Locate every Plasmodium ovale-infected red blood cell.
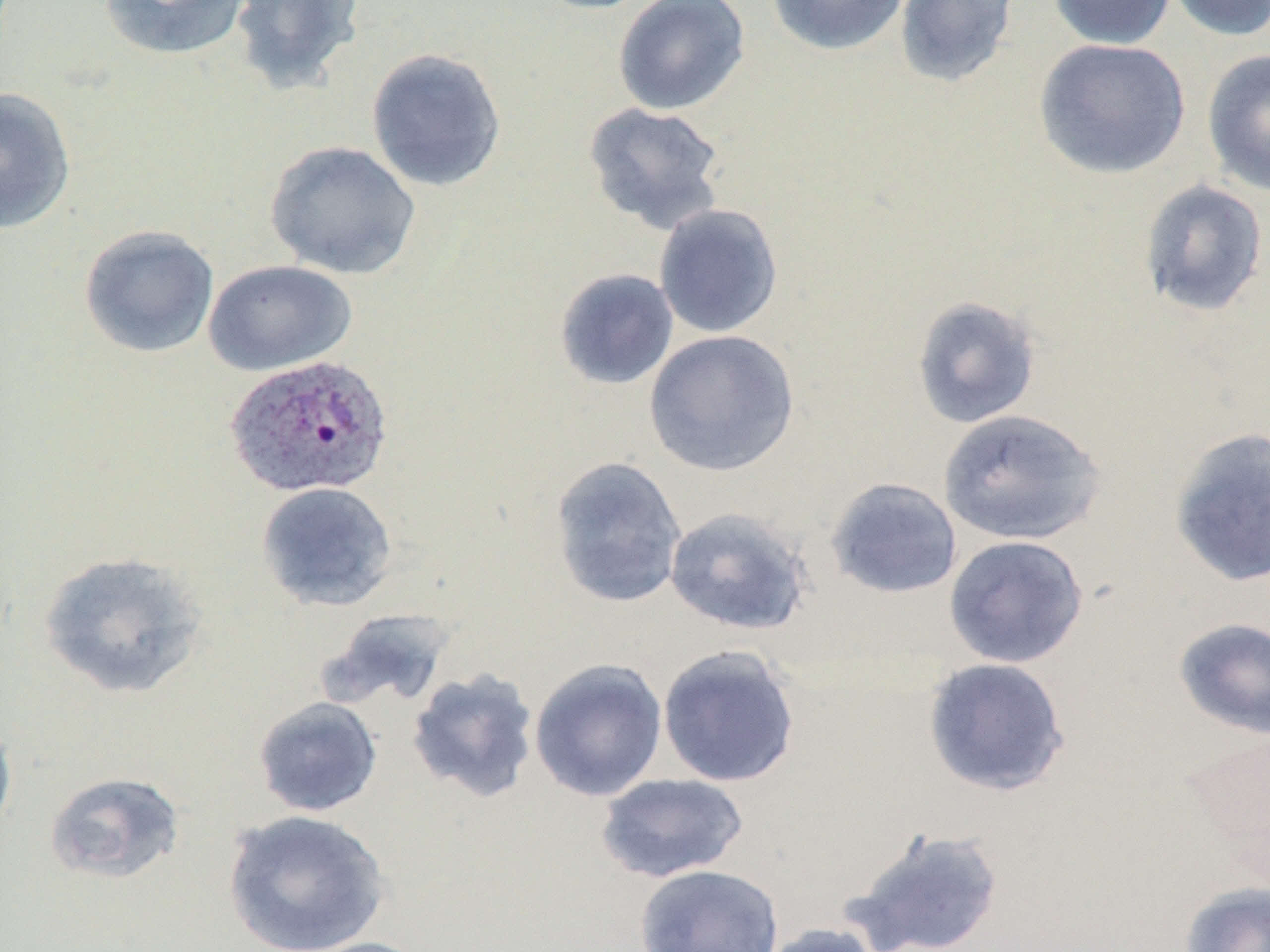

Approximate bounding boxes as (x1,y1)-(x2,y2) corner pairs in pixels.
Plasmodium ovale-infected red blood cells: (225,353)-(394,498).

Uninfected red blood cell locations: (98,0)-(252,62), (229,0)-(367,96), (528,0)-(658,14), (613,0)-(750,116), (765,0)-(910,57), (894,0)-(1020,88), (1047,0)-(1177,49), (1165,0)-(1270,42), (1033,37)-(1191,179), (365,47)-(507,192), (1202,48)-(1270,198), (0,86)-(77,235), (583,102)-(727,234), (264,140)-(421,280), (1138,179)-(1269,318), (653,203)-(784,338), (79,224)-(220,358), (203,260)-(358,376), (553,268)-(679,391), (911,295)-(1042,429), (643,329)-(800,477), (937,407)-(1105,546), (1168,426)-(1270,588), (548,455)-(688,609), (825,477)-(962,599), (256,481)-(398,611), (663,506)-(813,636), (943,535)-(1088,668), (38,550)-(208,700), (322,606)-(458,710), (1172,617)-(1270,739), (657,645)-(801,788), (921,656)-(1071,797), (529,657)-(668,802), (406,668)-(540,802), (253,696)-(383,817), (0,713)-(17,843), (1181,726)-(1270,873), (44,771)-(185,884), (596,773)-(749,883), (222,809)-(390,952), (843,826)-(1006,952), (635,863)-(785,952), (1179,881)-(1270,952), (758,922)-(886,952), (297,936)-(437,952). Slide-level diagnosis: Plasmodium ovale. May-Grünwald-Giemsa stain. Optical microscopy. 1000x magnification. Single field of view. Thin blood smear. Image is 1270×952 pixels.